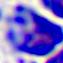

A leukocyte is shown. Captured at 400x magnification. Photomicrograph.